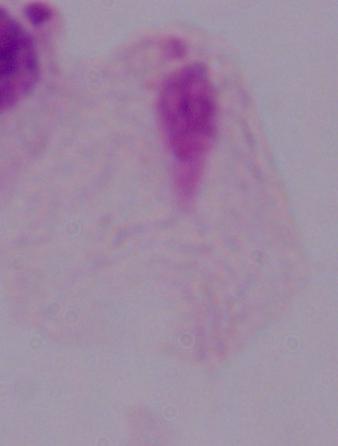 Captured at 1000x magnification. A trichomonad is shown. Micrograph.